Identify the blood parasite species.
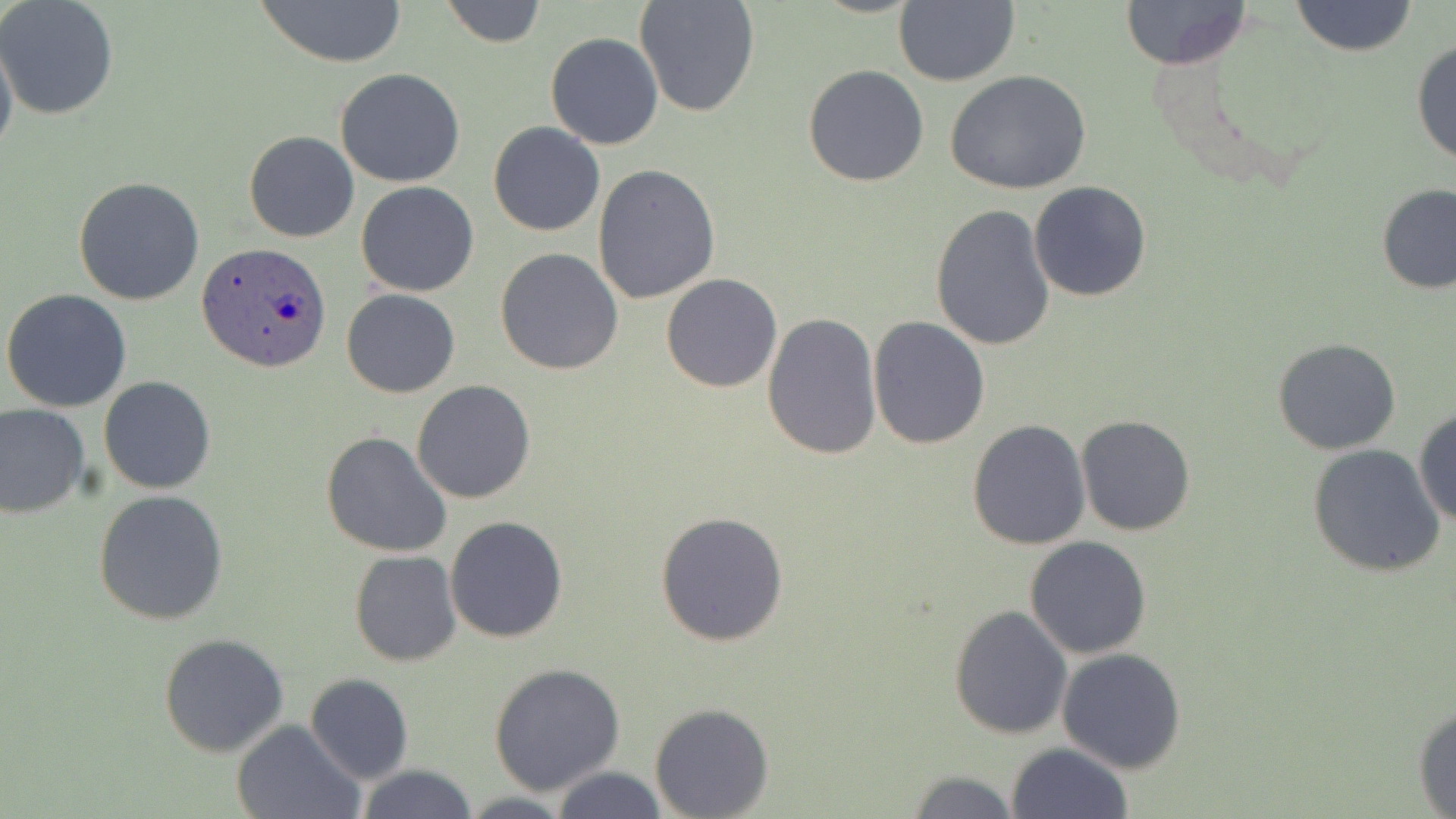
Plasmodium ovale.

Approximate bounding boxes as (x1, y1, x2, y2) in pixels. Plasmodium ovale-infected red blood cell locations: (199, 244, 333, 374). Uninfected red blood cell locations: (254, 0, 408, 68), (439, 0, 545, 48), (634, 0, 761, 118), (894, 0, 1019, 86), (1119, 0, 1252, 70), (1291, 0, 1418, 58), (0, 1, 119, 120), (0, 29, 19, 166), (544, 32, 665, 150), (1410, 39, 1456, 166), (802, 64, 930, 187), (335, 68, 466, 187), (946, 71, 1093, 196), (488, 121, 606, 236), (243, 130, 360, 243), (591, 162, 722, 305), (74, 175, 205, 305), (1028, 181, 1151, 302), (355, 182, 479, 297), (1375, 182, 1456, 295), (930, 203, 1056, 350), (495, 247, 623, 376), (661, 272, 782, 392), (2, 288, 132, 412), (341, 288, 460, 398), (762, 309, 884, 461), (868, 316, 992, 449), (1271, 337, 1402, 456), (98, 376, 216, 494), (410, 380, 537, 504), (0, 402, 91, 519), (1412, 406, 1456, 527), (1076, 415, 1196, 535), (967, 419, 1092, 551), (321, 430, 453, 560), (1307, 444, 1448, 579), (94, 488, 229, 625), (654, 512, 790, 646), (444, 515, 569, 644), (344, 534, 564, 657), (1024, 537, 1152, 659), (350, 551, 463, 666), (948, 604, 1072, 741), (159, 633, 289, 758), (1057, 647, 1187, 774), (488, 662, 625, 794), (305, 673, 414, 784), (1413, 699, 1456, 817), (650, 704, 773, 818), (232, 720, 367, 819), (1006, 743, 1131, 819), (355, 764, 479, 819), (547, 766, 668, 819), (905, 771, 1021, 818), (455, 793, 576, 819). Captured at 1000x magnification. Thin blood smear. May-Grünwald-Giemsa-stained preparation. One field of a larger specimen. Image is 1456×819 pixels. Optical microscopy.